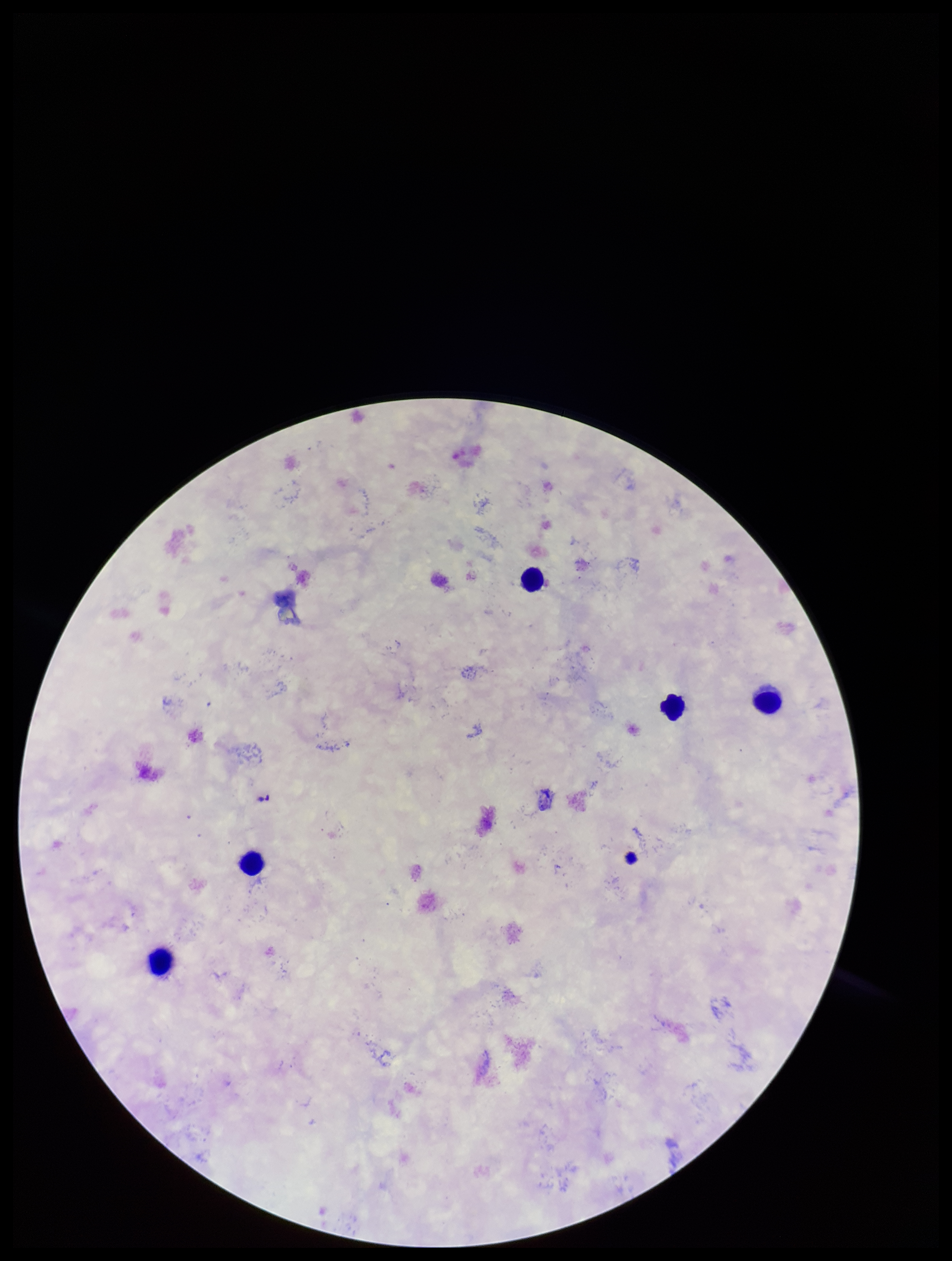
Parasite count: 0. Smartphone photograph taken through the eyepiece of a microscope. Stained with Giemsa. Preparation: thick blood smear. Leukocyte count: 5. Plasmodium parasites: none detected. One field from this slide. Image is 952×1261 pixels. Species reported for this patient: Plasmodium falciparum. Patient malaria status: infected.